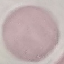 Malaria status: uninfected. Photographed with a smartphone camera at the microscope eyepiece. Automatically extracted cell patch, resized to 64 × 64 pixels. Thin blood film. Giemsa stain.